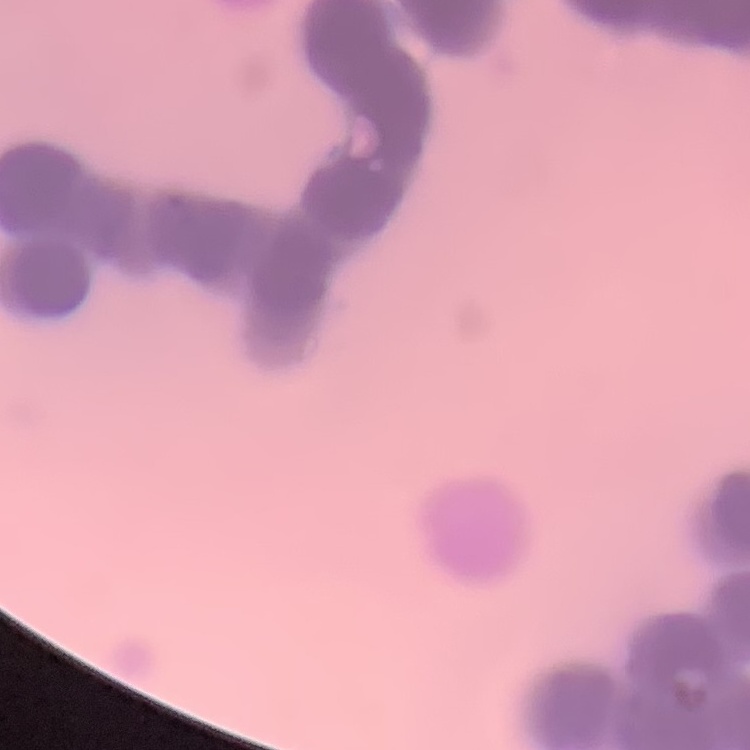
erythrocyte morphology = rouleaux formation
image type = square crop of a larger photomicrograph
preparation = thin peripheral smear
stain = Field's or Giemsa